Report the malaria status of this cell.
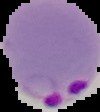

It is parasitized.

Segmented cell region on a black background. Image is 100×112 pixels. From a thin blood film.